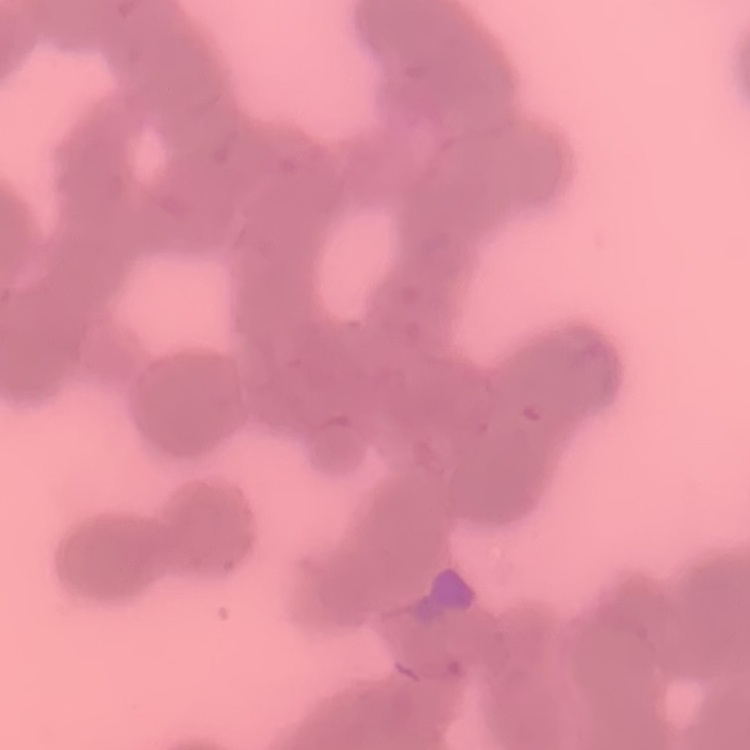
Summary:
  - Red blood cell morphology: rouleaux formation
  - Preparation: thin peripheral smear
  - Image type: square crop of a larger photomicrograph
  - Stain: Field's or Giemsa